State the blood parasite species.
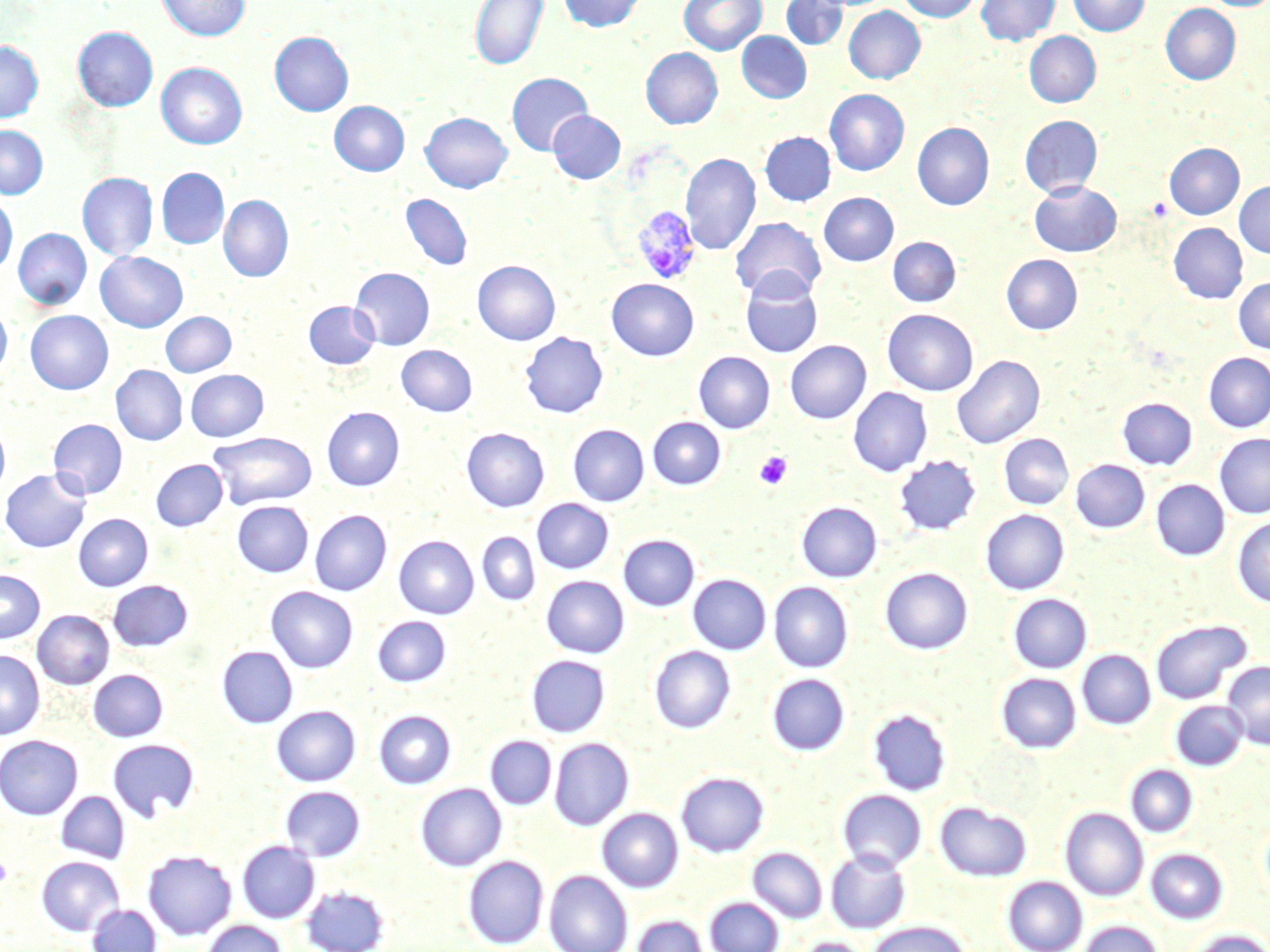

Plasmodium vivax.

{
  "preparation": "thin blood smear",
  "platelet_locations": "approximate bounding boxes as named x1/y1/x2/y2 corners in pixels: (x1=754, y1=451, x2=792, y2=490), (x1=0, y1=856, x2=12, y2=887)",
  "field_of_view": "one of a larger specimen",
  "plasmodium_vivax_infected_red_blood_cell_locations": "approximate bounding boxes as named x1/y1/x2/y2 corners in pixels: (x1=632, y1=206, x2=702, y2=285)",
  "uninfected_red_blood_cell_locations": "approximate bounding boxes as named x1/y1/x2/y2 corners in pixels: (x1=157, y1=0, x2=249, y2=41), (x1=470, y1=0, x2=548, y2=70), (x1=559, y1=0, x2=646, y2=32), (x1=679, y1=0, x2=766, y2=55), (x1=781, y1=0, x2=847, y2=50), (x1=898, y1=0, x2=981, y2=22), (x1=976, y1=0, x2=1060, y2=46), (x1=1068, y1=0, x2=1150, y2=36), (x1=1204, y1=0, x2=1270, y2=10), (x1=1161, y1=3, x2=1241, y2=85), (x1=843, y1=6, x2=924, y2=83), (x1=73, y1=27, x2=158, y2=111), (x1=269, y1=31, x2=353, y2=116), (x1=737, y1=31, x2=811, y2=103), (x1=1024, y1=32, x2=1101, y2=107), (x1=0, y1=41, x2=43, y2=122), (x1=641, y1=47, x2=722, y2=129), (x1=156, y1=62, x2=247, y2=149), (x1=507, y1=73, x2=593, y2=156), (x1=824, y1=89, x2=909, y2=176), (x1=329, y1=101, x2=409, y2=176), (x1=548, y1=111, x2=625, y2=184), (x1=421, y1=112, x2=512, y2=193), (x1=1020, y1=115, x2=1102, y2=198), (x1=912, y1=122, x2=994, y2=210), (x1=0, y1=125, x2=48, y2=199), (x1=760, y1=132, x2=836, y2=206), (x1=1165, y1=143, x2=1244, y2=219), (x1=681, y1=153, x2=760, y2=255), (x1=157, y1=168, x2=229, y2=249), (x1=77, y1=172, x2=157, y2=262), (x1=1029, y1=181, x2=1122, y2=257), (x1=1234, y1=181, x2=1270, y2=258), (x1=401, y1=193, x2=472, y2=270), (x1=819, y1=193, x2=899, y2=266), (x1=0, y1=195, x2=17, y2=275), (x1=219, y1=195, x2=293, y2=282), (x1=731, y1=217, x2=825, y2=301), (x1=1169, y1=223, x2=1248, y2=304), (x1=13, y1=228, x2=91, y2=310), (x1=888, y1=237, x2=960, y2=307), (x1=96, y1=252, x2=187, y2=332), (x1=1001, y1=255, x2=1082, y2=335), (x1=473, y1=260, x2=560, y2=345), (x1=350, y1=267, x2=434, y2=350), (x1=740, y1=271, x2=823, y2=359), (x1=1233, y1=277, x2=1270, y2=353), (x1=607, y1=279, x2=699, y2=360), (x1=304, y1=301, x2=378, y2=369), (x1=0, y1=304, x2=11, y2=380), (x1=883, y1=309, x2=978, y2=396), (x1=25, y1=310, x2=113, y2=394), (x1=161, y1=312, x2=236, y2=377), (x1=520, y1=332, x2=608, y2=419), (x1=785, y1=340, x2=871, y2=424), (x1=397, y1=345, x2=477, y2=416), (x1=694, y1=352, x2=775, y2=433), (x1=1203, y1=353, x2=1270, y2=432), (x1=952, y1=355, x2=1045, y2=449), (x1=110, y1=365, x2=187, y2=445), (x1=186, y1=369, x2=268, y2=441), (x1=848, y1=387, x2=932, y2=477), (x1=1117, y1=397, x2=1197, y2=470), (x1=322, y1=407, x2=404, y2=491), (x1=647, y1=417, x2=726, y2=490), (x1=48, y1=419, x2=127, y2=499), (x1=0, y1=423, x2=10, y2=499), (x1=568, y1=424, x2=648, y2=506), (x1=462, y1=428, x2=549, y2=512), (x1=209, y1=431, x2=317, y2=509), (x1=1214, y1=433, x2=1270, y2=518), (x1=999, y1=434, x2=1073, y2=509), (x1=894, y1=455, x2=980, y2=535), (x1=151, y1=459, x2=227, y2=531), (x1=1071, y1=459, x2=1150, y2=533), (x1=1, y1=469, x2=91, y2=553), (x1=1151, y1=479, x2=1229, y2=560), (x1=532, y1=499, x2=613, y2=573), (x1=232, y1=501, x2=313, y2=577), (x1=797, y1=502, x2=881, y2=582), (x1=981, y1=509, x2=1069, y2=595), (x1=310, y1=510, x2=391, y2=596), (x1=74, y1=514, x2=153, y2=591), (x1=1232, y1=516, x2=1270, y2=608), (x1=477, y1=532, x2=540, y2=606), (x1=619, y1=534, x2=700, y2=611), (x1=394, y1=536, x2=478, y2=619), (x1=880, y1=567, x2=973, y2=654), (x1=0, y1=570, x2=45, y2=643), (x1=688, y1=574, x2=771, y2=654), (x1=542, y1=575, x2=628, y2=658), (x1=108, y1=580, x2=193, y2=651), (x1=769, y1=582, x2=853, y2=672), (x1=266, y1=586, x2=358, y2=673), (x1=1008, y1=593, x2=1091, y2=673), (x1=32, y1=610, x2=114, y2=689), (x1=372, y1=616, x2=450, y2=687), (x1=1151, y1=619, x2=1250, y2=704), (x1=649, y1=645, x2=735, y2=733), (x1=217, y1=646, x2=297, y2=728), (x1=1077, y1=649, x2=1155, y2=729), (x1=0, y1=650, x2=44, y2=739), (x1=527, y1=655, x2=610, y2=737), (x1=1222, y1=661, x2=1270, y2=749), (x1=88, y1=669, x2=168, y2=741), (x1=767, y1=673, x2=849, y2=756), (x1=996, y1=673, x2=1081, y2=753), (x1=1171, y1=700, x2=1247, y2=770), (x1=272, y1=705, x2=360, y2=786), (x1=869, y1=708, x2=950, y2=795), (x1=374, y1=709, x2=456, y2=789), (x1=0, y1=735, x2=83, y2=819), (x1=485, y1=735, x2=556, y2=809), (x1=107, y1=737, x2=200, y2=822), (x1=549, y1=738, x2=633, y2=830), (x1=1126, y1=765, x2=1198, y2=837), (x1=676, y1=771, x2=768, y2=857), (x1=416, y1=783, x2=506, y2=871), (x1=280, y1=785, x2=366, y2=861), (x1=838, y1=789, x2=926, y2=871), (x1=56, y1=791, x2=129, y2=863), (x1=935, y1=801, x2=1031, y2=881), (x1=1060, y1=807, x2=1148, y2=901), (x1=598, y1=808, x2=683, y2=892), (x1=1259, y1=818, x2=1270, y2=903), (x1=237, y1=841, x2=319, y2=923), (x1=748, y1=847, x2=827, y2=923), (x1=1146, y1=848, x2=1227, y2=924), (x1=143, y1=850, x2=237, y2=940), (x1=826, y1=850, x2=910, y2=932), (x1=463, y1=855, x2=548, y2=948), (x1=36, y1=856, x2=124, y2=935), (x1=544, y1=870, x2=632, y2=952), (x1=1003, y1=876, x2=1087, y2=952), (x1=300, y1=884, x2=390, y2=952), (x1=705, y1=897, x2=783, y2=952), (x1=88, y1=904, x2=161, y2=952), (x1=632, y1=915, x2=709, y2=952), (x1=201, y1=920, x2=287, y2=952), (x1=865, y1=921, x2=971, y2=952), (x1=1079, y1=921, x2=1163, y2=952), (x1=1186, y1=930, x2=1270, y2=952), (x1=797, y1=937, x2=871, y2=952)",
  "modality": "optical microscopy",
  "magnification": "1000x",
  "stain": "May-Grünwald-Giemsa",
  "image_size": "1270×952 pixels"
}